Assess this cell for malaria.
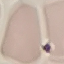
It is uninfected.

Summary:
  - Preparation: thin blood smear
  - Stain: Giemsa
  - Capture: smartphone camera at the microscope eyepiece
  - Image type: automatically extracted cell patch, resized to 64 × 64 pixels